Classify this cell by malaria status.
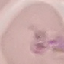

It is parasitized.

Acquired by smartphone through the microscope eyepiece. Cell patch, automatically extracted from a larger field of view and resized to 64 × 64 pixels. Thin blood film. Giemsa-stained preparation.